Identify the cell.
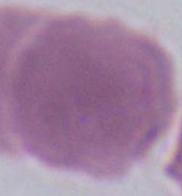

This is an erythrocyte.

{
  "modality": "photomicrograph",
  "magnification": "1000x"
}